Name the blood parasite species.
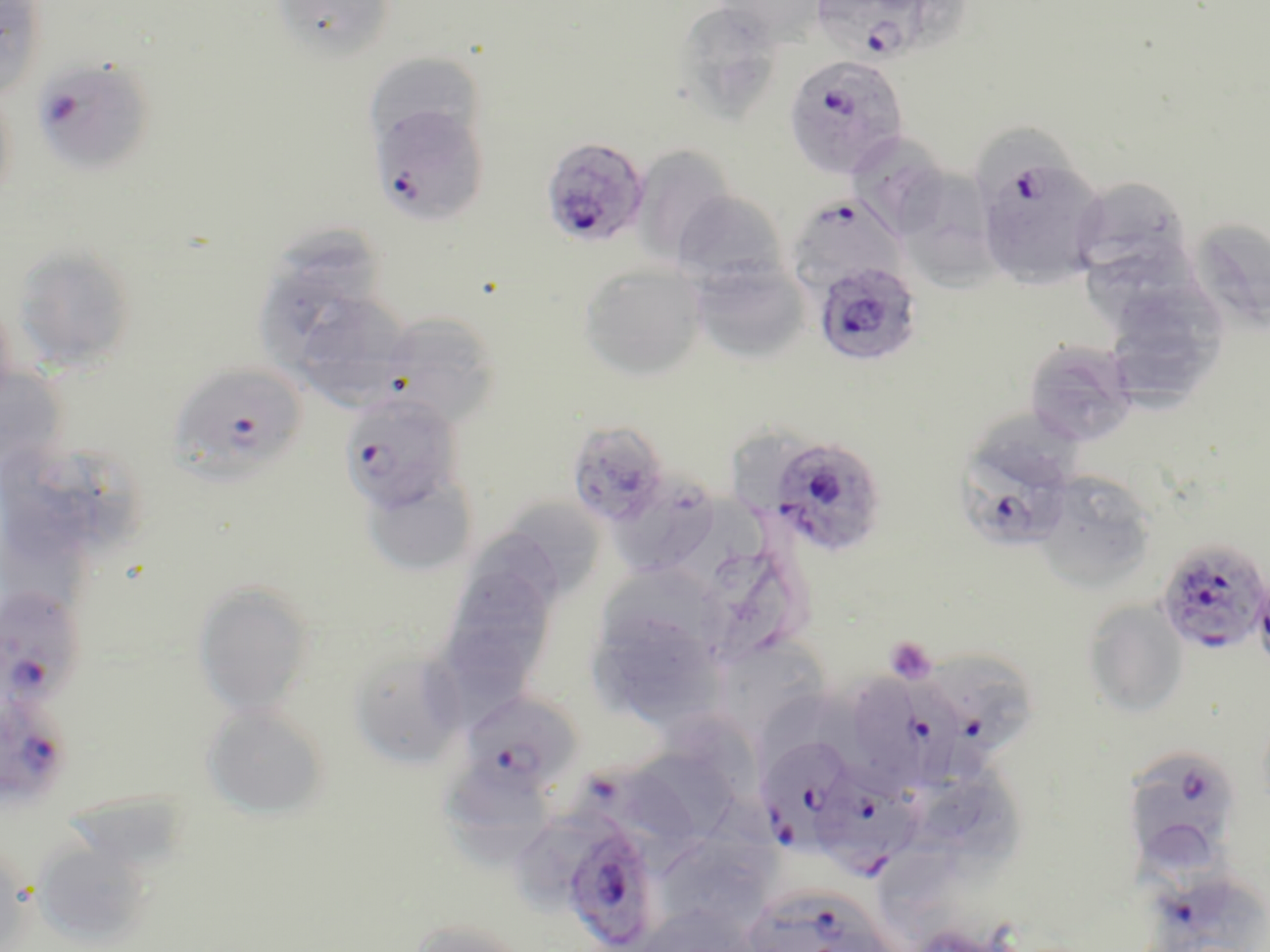
Plasmodium falciparum.

Summary:
  - Coordinate format: approximate bounding boxes as (x1,y1)-(x2,y2) corner pairs in pixels
  - Uninfected red blood cell locations: (0,0)-(48,99), (270,0)-(398,62), (711,0)-(829,43), (669,3)-(786,124), (365,52)-(486,152), (0,78)-(17,210), (974,126)-(1081,197), (854,140)-(947,236), (630,143)-(739,265), (901,174)-(1003,294), (1071,174)-(1194,288), (671,191)-(791,292), (1189,217)-(1270,334), (1087,235)-(1208,325), (11,243)-(137,373), (688,261)-(811,364), (579,264)-(707,381), (258,271)-(361,365), (1115,286)-(1232,372), (307,298)-(410,408), (376,312)-(503,429), (1113,319)-(1208,413), (1024,339)-(1138,447), (0,357)-(68,473), (565,419)-(672,530), (33,442)-(141,557), (359,468)-(479,577), (1031,472)-(1159,593), (610,484)-(719,572), (702,491)-(770,572), (515,501)-(603,593), (0,509)-(90,622), (479,530)-(561,610), (707,553)-(792,659), (439,559)-(563,699), (598,572)-(721,652), (193,580)-(316,719), (1081,600)-(1189,718), (587,604)-(724,730), (712,637)-(833,741), (347,646)-(469,770), (764,686)-(864,775), (201,703)-(330,820), (664,712)-(757,797), (632,749)-(739,844), (439,773)-(552,873), (928,777)-(1026,878), (68,787)-(186,867), (667,802)-(780,925), (31,838)-(154,948), (880,850)-(980,952), (404,918)-(534,952)
  - Platelet locations: (885,635)-(938,684)
  - Plasmodium falciparum-infected red blood cell locations: (806,0)-(951,66), (783,53)-(909,179), (30,56)-(156,178), (367,103)-(490,227), (540,137)-(650,248), (974,149)-(1107,289), (786,193)-(906,295), (812,261)-(923,367), (170,362)-(307,485), (338,392)-(464,513), (954,430)-(1076,553), (766,434)-(887,558), (1155,537)-(1270,656), (0,589)-(87,712), (939,654)-(1030,762), (860,676)-(965,794), (0,687)-(75,809), (459,689)-(583,798), (758,735)-(859,846), (1120,748)-(1243,869), (573,766)-(702,853), (811,771)-(922,879), (557,819)-(662,952), (1125,824)-(1230,936), (739,882)-(901,952)
  - Field of view: single
  - Stain: May-Grünwald-Giemsa
  - Image size: 1270×952 pixels
  - Magnification: 1000x
  - Modality: optical microscopy
  - Preparation: thin blood smear